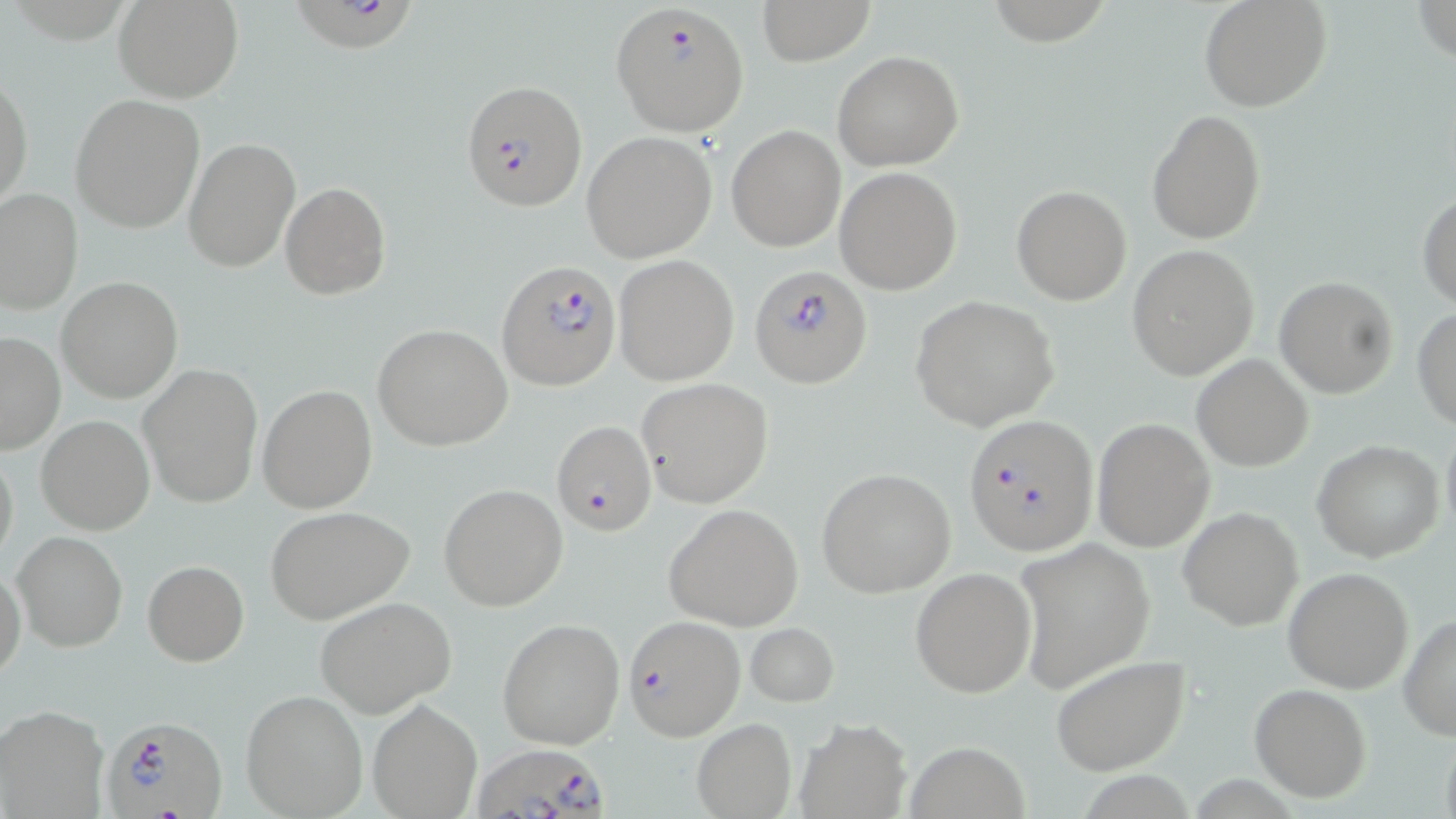 Approximate bounding boxes as (x1,y1)-(x2,y2) corner pairs in pixels. Plasmodium falciparum-infected red blood cell locations: (295,0)-(428,62), (613,3)-(748,136), (458,79)-(587,213), (499,261)-(622,390), (749,266)-(872,388), (965,414)-(1098,558), (552,421)-(657,536), (623,616)-(744,739), (104,716)-(227,819), (472,745)-(614,819). Uninfected red blood cell locations: (113,0)-(242,103), (755,0)-(876,66), (1198,0)-(1332,112), (1413,0)-(1456,72), (832,52)-(964,171), (0,73)-(32,209), (69,94)-(204,233), (1147,108)-(1266,246), (727,126)-(846,252), (580,132)-(716,262), (182,138)-(300,272), (834,166)-(962,294), (280,183)-(390,299), (1012,185)-(1132,305), (0,187)-(82,317), (1416,189)-(1456,310), (1125,245)-(1259,378), (613,255)-(739,385), (55,276)-(184,404), (1273,276)-(1399,398), (909,294)-(1061,433), (1412,306)-(1456,430), (371,324)-(512,450), (0,331)-(66,454), (1192,354)-(1314,471), (139,364)-(264,510), (639,379)-(774,506), (257,384)-(378,515), (35,415)-(156,536), (1091,418)-(1215,551), (1440,424)-(1456,543), (0,440)-(19,566), (1312,440)-(1445,564), (816,468)-(956,596), (438,484)-(568,611), (665,503)-(805,630), (1177,506)-(1303,631), (267,507)-(413,624), (10,531)-(128,653), (1012,536)-(1155,695), (142,561)-(249,666), (1,566)-(26,685), (1283,566)-(1414,693), (910,567)-(1037,699), (315,598)-(458,717), (1398,612)-(1456,740), (497,618)-(625,749), (744,621)-(840,707), (1050,654)-(1192,774), (1249,683)-(1371,802), (240,689)-(368,818), (369,698)-(482,819), (1,704)-(108,817), (691,718)-(797,818), (796,719)-(912,818), (906,739)-(1031,817). Slide-level diagnosis: Plasmodium falciparum. One field of a larger specimen. Optical microscopy. May-Grünwald-Giemsa-stained preparation. Thin blood film. Image is 1456×819 pixels. 1000x magnification.